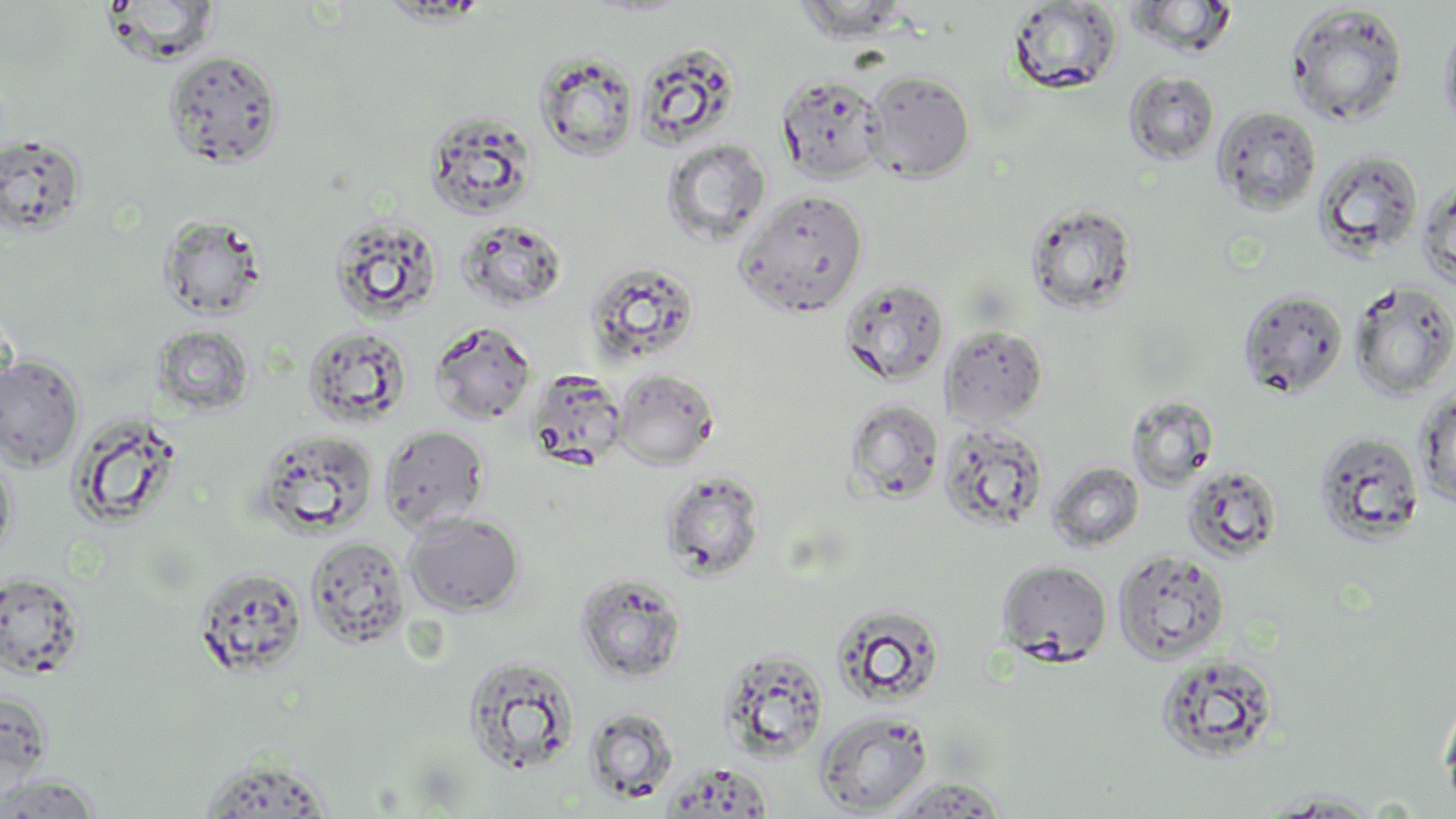

{
  "slide_level_diagnosis": "negative for blood parasites",
  "image_size": "1456×819 pixels",
  "stain": "May-Grünwald-Giemsa",
  "modality": "light microscopy",
  "magnification": "1000x",
  "uninfected_red_blood_cell_locations": "approximate bounding boxes as (x1,y1)-(x2,y2) corner pairs in pixels: (103,0)-(220,66), (794,0)-(913,43), (1124,0)-(1239,58), (1005,1)-(1122,95), (1285,3)-(1409,127), (1438,15)-(1456,141), (635,43)-(740,147), (535,50)-(639,161), (163,51)-(284,169), (863,70)-(975,182), (1123,70)-(1221,165), (776,74)-(887,183), (1211,105)-(1322,215), (424,110)-(539,220), (0,135)-(87,238), (661,139)-(772,247), (1315,150)-(1423,261), (1417,178)-(1456,290), (736,189)-(869,317), (1024,201)-(1139,315), (157,213)-(268,321), (328,214)-(444,323), (457,218)-(569,314), (584,260)-(701,365), (839,276)-(950,386), (1349,280)-(1456,400), (1238,288)-(1349,398), (429,321)-(537,425), (151,324)-(254,416), (941,324)-(1049,426), (302,325)-(412,428), (0,355)-(85,473), (525,367)-(629,471), (613,369)-(719,469), (1415,387)-(1456,509), (1126,395)-(1219,491), (844,399)-(944,504), (66,412)-(183,531), (939,420)-(1050,533), (379,423)-(490,533), (253,427)-(379,539), (1315,432)-(1424,544), (0,445)-(17,564), (1049,462)-(1144,553), (1181,464)-(1283,563), (661,469)-(766,581), (405,512)-(525,616), (305,535)-(411,649), (1113,549)-(1230,663), (996,559)-(1112,664), (193,565)-(308,678), (0,572)-(85,678), (573,572)-(688,685), (831,603)-(948,707), (717,648)-(830,762), (1155,653)-(1280,762), (461,654)-(581,775), (0,689)-(53,793), (1438,694)-(1456,814), (583,707)-(679,804), (815,710)-(933,816), (195,757)-(339,817), (1,774)-(103,818), (882,777)-(1011,817), (1259,792)-(1388,817)",
  "preparation": "thin blood smear",
  "field_of_view": "single"
}